Report the malaria status of this cell.
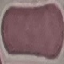
It is uninfected.

Summary:
  - Image type: automatically extracted cell patch, resized to 64 × 64 pixels
  - Preparation: thin blood smear
  - Capture: smartphone camera at the microscope eyepiece
  - Stain: Giemsa